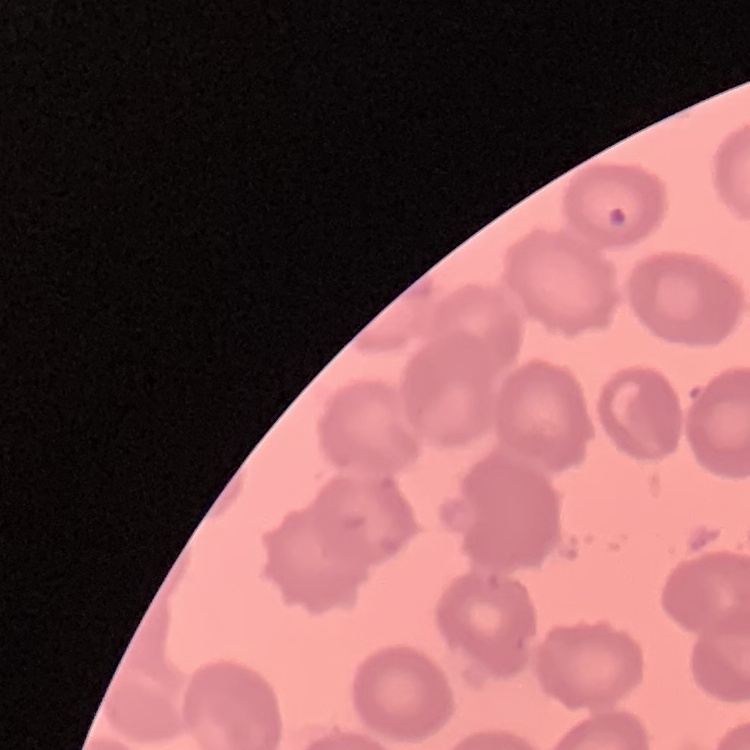

Summary:
  - Erythrocyte morphology: no rouleaux formation
  - Preparation: thin blood smear
  - Image type: square crop of a larger photomicrograph
  - Stain: Field's or Giemsa